Identify the cell.
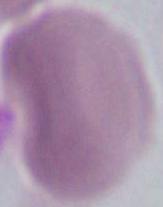

This is an erythrocyte.

1000x magnification. Photomicrograph.